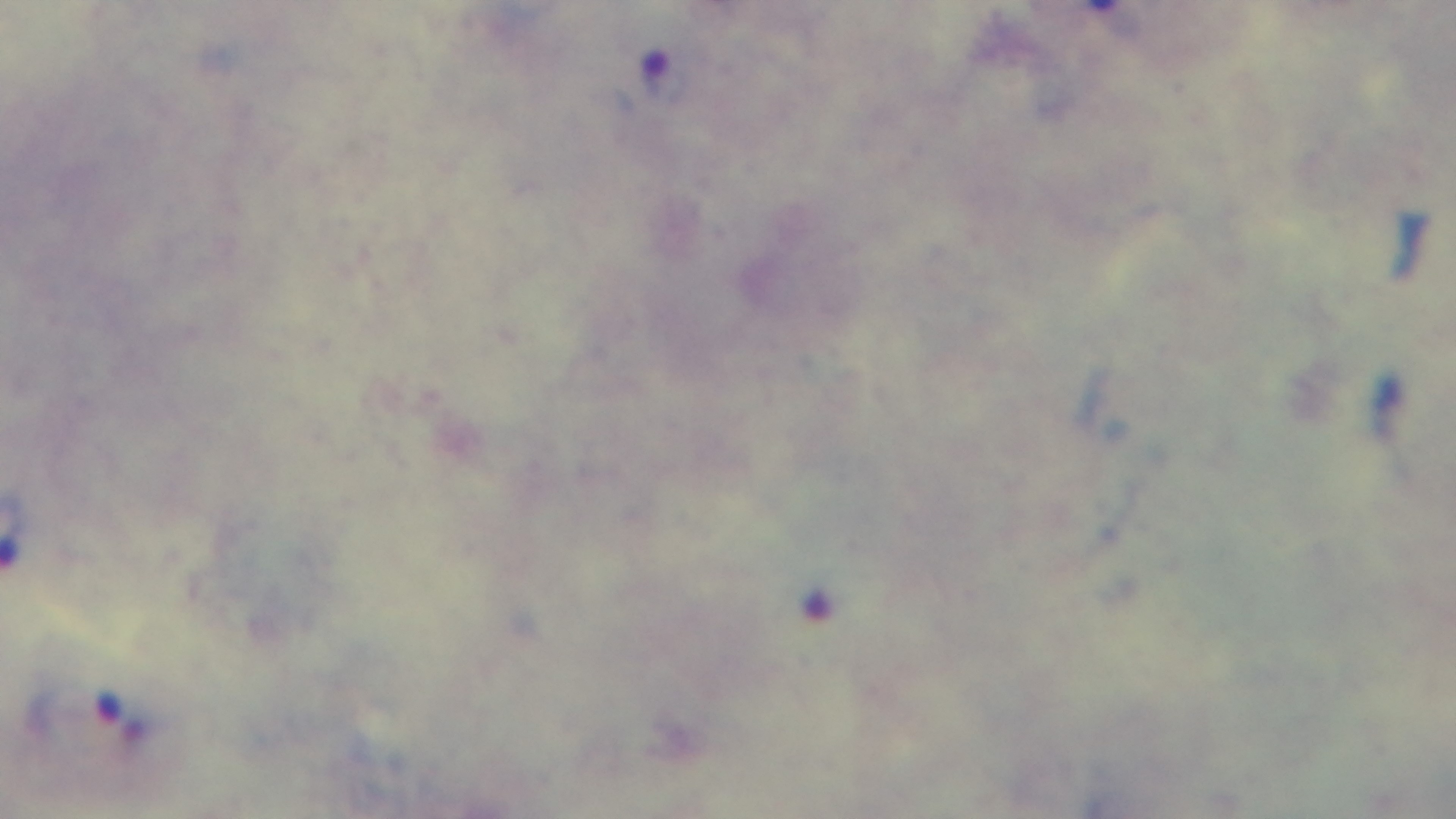

stain = Giemsa
preparation = thick blood film
modality = light microscopy
malaria status = infected
objective = 100x oil immersion
capture = mounted 4K digital camera
field of view = one from the slide